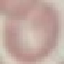
Result: negative for malaria parasites. Photographed with a smartphone camera at the microscope eyepiece. Automatically extracted cell patch, resized to 64 × 64 pixels. Thin smear of blood. Giemsa-stained preparation.